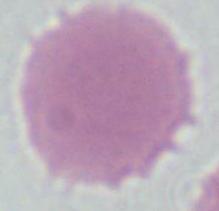
{
  "modality": "photomicrograph",
  "magnification": "1000x",
  "identification": "red blood cell"
}